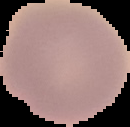
Summary:
  - Image type: segmented cell region with the area outside set to black
  - Preparation: thin blood film
  - Image size: 130×127 pixels
  - Malaria status: uninfected